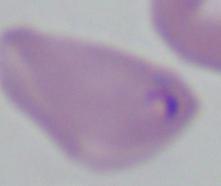

Summary:
  - Modality: micrograph
  - Magnification: 1000x
  - Identification: Babesia